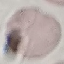

result = no malaria parasites detected
stain = Giemsa
image type = cell patch, automatically extracted from a larger field of view and resized to 64 × 64 pixels
preparation = thin smear
capture = smartphone through the microscope eyepiece